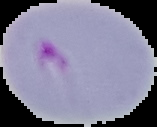

Cell region segmented out of the field of view; the surrounding area is masked to black. From a thin blood film. Image is 157×127 pixels. Malaria status: parasitized.